Identify the parasite.
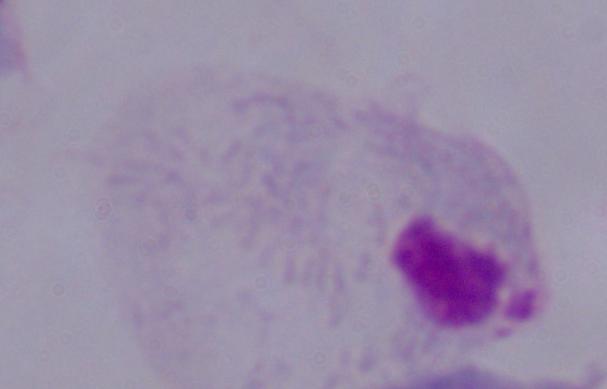

This is a trichomonad.

1000x magnification. Photomicrograph.